Name the cell type shown.
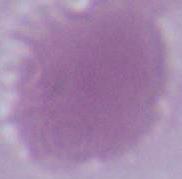
This is an erythrocyte.

Micrograph. 1000x magnification.